Identify the parasite.
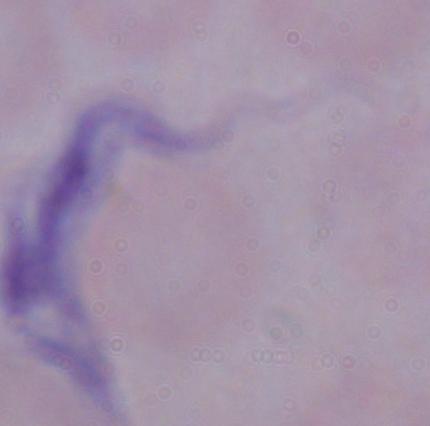
This is a trypanosome.

modality = micrograph
magnification = 1000x